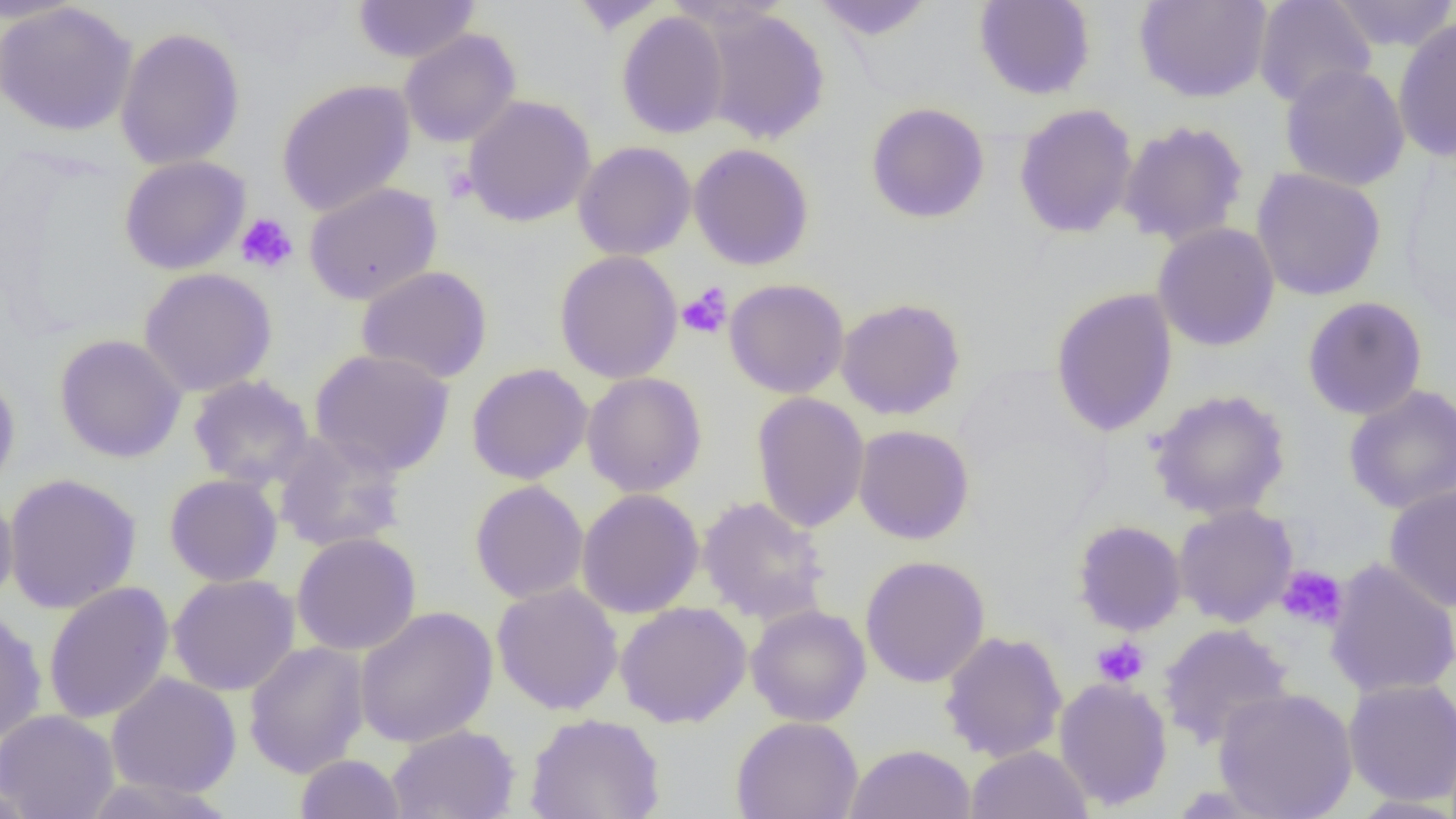

slide_level_diagnosis: no evidence of blood parasites
uninfected_red_blood_cell_locations: 'approximate bounding boxes as named x1/y1/x2/y2 corners in pixels: (x1=352, y1=0, x2=481, y2=64), (x1=566, y1=0, x2=668, y2=34), (x1=810, y1=0, x2=936, y2=40), (x1=973, y1=0, x2=1096, y2=100), (x1=1135, y1=0, x2=1273, y2=103), (x1=1253, y1=0, x2=1377, y2=109), (x1=1329, y1=0, x2=1456, y2=53), (x1=1, y1=2, x2=138, y2=136), (x1=699, y1=7, x2=831, y2=145), (x1=616, y1=11, x2=730, y2=139), (x1=1393, y1=16, x2=1456, y2=163), (x1=115, y1=27, x2=246, y2=170), (x1=399, y1=29, x2=521, y2=148), (x1=1279, y1=63, x2=1410, y2=191), (x1=275, y1=79, x2=416, y2=217), (x1=461, y1=94, x2=596, y2=227), (x1=865, y1=102, x2=990, y2=224), (x1=1013, y1=103, x2=1139, y2=239), (x1=1118, y1=120, x2=1249, y2=247), (x1=573, y1=141, x2=697, y2=261), (x1=688, y1=143, x2=815, y2=271), (x1=119, y1=155, x2=251, y2=275), (x1=1250, y1=168, x2=1387, y2=301), (x1=303, y1=182, x2=442, y2=305), (x1=1152, y1=222, x2=1280, y2=352), (x1=554, y1=250, x2=683, y2=384), (x1=356, y1=265, x2=493, y2=384), (x1=138, y1=267, x2=278, y2=396), (x1=723, y1=278, x2=850, y2=398), (x1=1049, y1=287, x2=1179, y2=437), (x1=1302, y1=296, x2=1428, y2=420), (x1=835, y1=297, x2=966, y2=420), (x1=54, y1=334, x2=188, y2=463), (x1=310, y1=349, x2=455, y2=476), (x1=466, y1=363, x2=593, y2=485), (x1=0, y1=368, x2=21, y2=495), (x1=581, y1=372, x2=708, y2=497), (x1=187, y1=375, x2=315, y2=490), (x1=1342, y1=384, x2=1456, y2=514), (x1=1148, y1=389, x2=1291, y2=520), (x1=751, y1=391, x2=869, y2=533), (x1=852, y1=425, x2=975, y2=545), (x1=272, y1=431, x2=409, y2=553), (x1=2, y1=472, x2=142, y2=614), (x1=164, y1=474, x2=283, y2=587), (x1=469, y1=480, x2=589, y2=604), (x1=1384, y1=485, x2=1456, y2=612), (x1=576, y1=488, x2=705, y2=619), (x1=0, y1=490, x2=18, y2=608), (x1=697, y1=495, x2=831, y2=625), (x1=1173, y1=503, x2=1298, y2=627), (x1=1072, y1=520, x2=1187, y2=636), (x1=292, y1=531, x2=422, y2=656), (x1=860, y1=554, x2=991, y2=688), (x1=1324, y1=559, x2=1456, y2=699), (x1=168, y1=574, x2=300, y2=696), (x1=43, y1=581, x2=174, y2=724), (x1=491, y1=582, x2=624, y2=715), (x1=614, y1=601, x2=752, y2=728), (x1=745, y1=604, x2=871, y2=727), (x1=354, y1=605, x2=498, y2=748), (x1=0, y1=608, x2=47, y2=744), (x1=1157, y1=623, x2=1295, y2=750), (x1=939, y1=630, x2=1068, y2=763), (x1=243, y1=640, x2=371, y2=778), (x1=106, y1=672, x2=242, y2=798), (x1=1054, y1=677, x2=1173, y2=811), (x1=1342, y1=678, x2=1456, y2=806), (x1=1213, y1=687, x2=1358, y2=819), (x1=0, y1=709, x2=119, y2=819), (x1=524, y1=712, x2=666, y2=819), (x1=731, y1=715, x2=864, y2=819), (x1=386, y1=724, x2=520, y2=819), (x1=844, y1=744, x2=977, y2=819), (x1=965, y1=745, x2=1093, y2=819), (x1=295, y1=753, x2=406, y2=819), (x1=80, y1=775, x2=236, y2=818), (x1=0, y1=780, x2=38, y2=819)'
modality: light microscopy
platelet_locations: 'approximate bounding boxes as named x1/y1/x2/y2 corners in pixels: (x1=235, y1=213, x2=298, y2=275), (x1=676, y1=284, x2=732, y2=339), (x1=1276, y1=565, x2=1348, y2=631), (x1=1091, y1=637, x2=1150, y2=688)'
field_of_view: one of a larger specimen
preparation: thin blood smear
image_size: 1456×819 pixels
magnification: 1000x